Outline each Plasmodium falciparum-infected red blood cell.
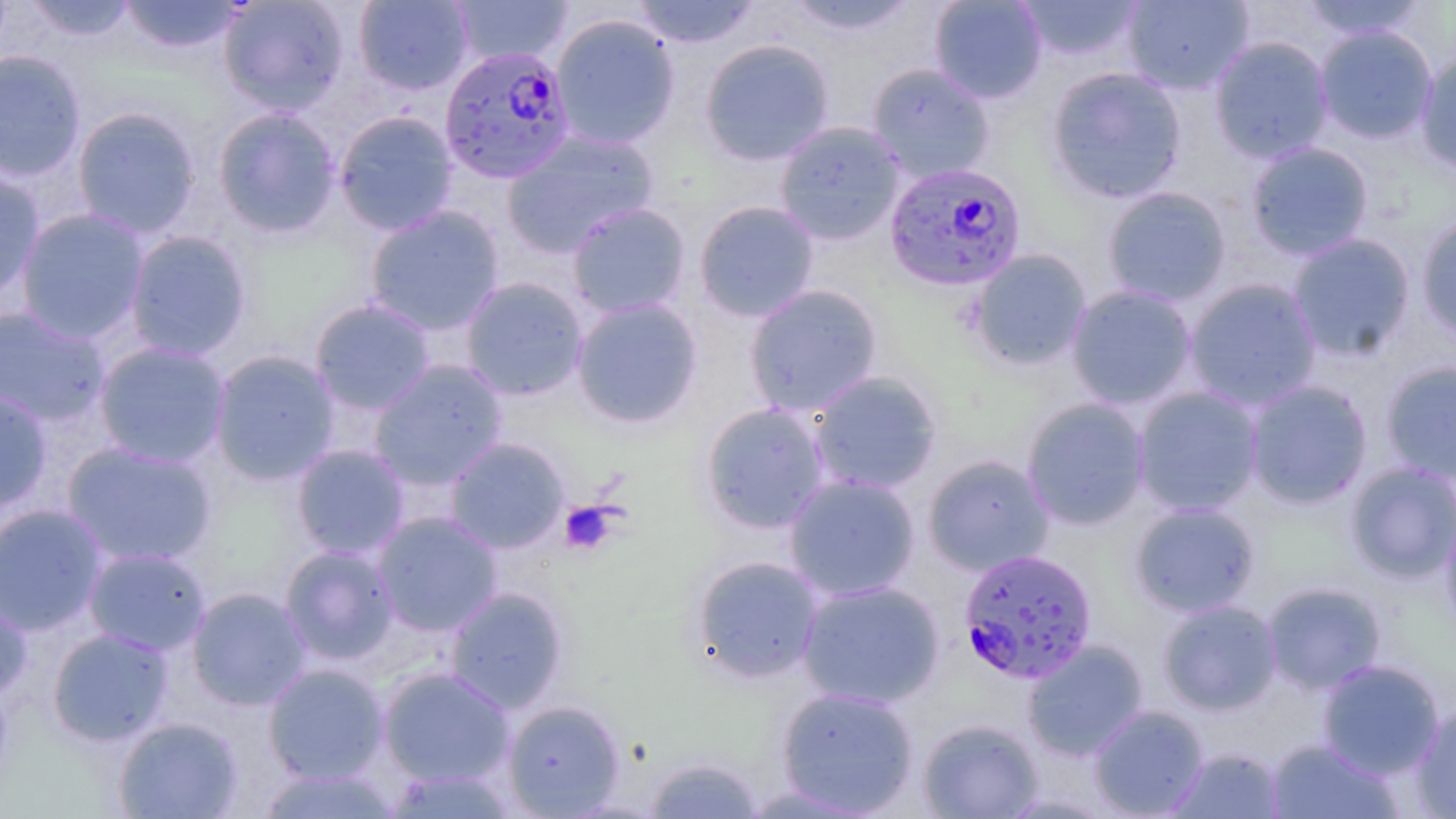
Approximate bounding boxes as (x1,y1)-(x2,y2) corner pairs in pixels.
Plasmodium falciparum-infected red blood cells: (438,45)-(575,183), (883,161)-(1028,292), (958,549)-(1097,684).

Summary:
  - Platelet locations: (558,500)-(620,555)
  - Uninfected red blood cell locations: (24,0)-(139,43), (117,0)-(246,54), (218,0)-(350,116), (353,0)-(473,95), (448,0)-(573,67), (630,0)-(761,48), (782,0)-(921,36), (929,0)-(1047,104), (1015,0)-(1144,62), (1122,0)-(1253,95), (1299,0)-(1428,41), (549,14)-(680,149), (1315,25)-(1438,144), (1209,35)-(1335,163), (699,38)-(835,167), (0,50)-(87,182), (1415,51)-(1456,175), (867,63)-(995,183), (1046,67)-(1187,204), (71,106)-(202,239), (213,106)-(341,238), (333,110)-(459,237), (774,121)-(905,245), (501,130)-(659,257), (1245,141)-(1374,261), (0,166)-(46,304), (1102,186)-(1232,307), (694,200)-(820,323), (566,202)-(691,319), (365,205)-(505,335), (14,207)-(150,343), (1416,216)-(1456,345), (124,230)-(252,362), (1287,232)-(1416,361), (967,248)-(1092,371), (460,276)-(589,401), (1184,278)-(1323,411), (744,284)-(884,417), (1065,285)-(1199,410), (570,298)-(704,430), (310,299)-(436,416), (0,305)-(111,427), (93,341)-(231,469), (209,349)-(340,485), (369,359)-(509,490), (1380,361)-(1456,484), (807,370)-(943,495), (1244,380)-(1373,509), (1132,386)-(1265,517), (0,387)-(53,515), (1022,397)-(1151,530), (697,401)-(832,535), (445,437)-(570,554), (61,441)-(217,568), (291,444)-(410,560), (923,454)-(1055,576), (1345,462)-(1456,583), (784,473)-(921,601), (1129,502)-(1261,618), (0,503)-(108,636), (372,511)-(503,637), (1441,513)-(1456,638), (280,545)-(400,665), (83,547)-(211,656), (689,554)-(825,684), (796,579)-(945,709), (1262,582)-(1387,695), (0,583)-(32,705), (444,586)-(569,714), (187,587)-(311,710), (1158,599)-(1282,715), (47,628)-(174,746), (1022,639)-(1149,760), (1317,659)-(1445,780), (262,663)-(389,784), (377,666)-(515,788), (776,686)-(919,816), (502,699)-(625,817), (1412,702)-(1456,818), (1089,705)-(1209,818), (113,716)-(243,818), (918,719)-(1044,818), (1265,739)-(1404,818), (1167,747)-(1286,818), (642,755)-(764,818), (256,765)-(401,818), (383,767)-(518,817)
  - Slide-level diagnosis: Plasmodium falciparum
  - Image size: 1456×819 pixels
  - Preparation: thin blood film
  - Stain: May-Grünwald-Giemsa
  - Field of view: one of a larger specimen
  - Magnification: 1000x
  - Modality: optical microscopy